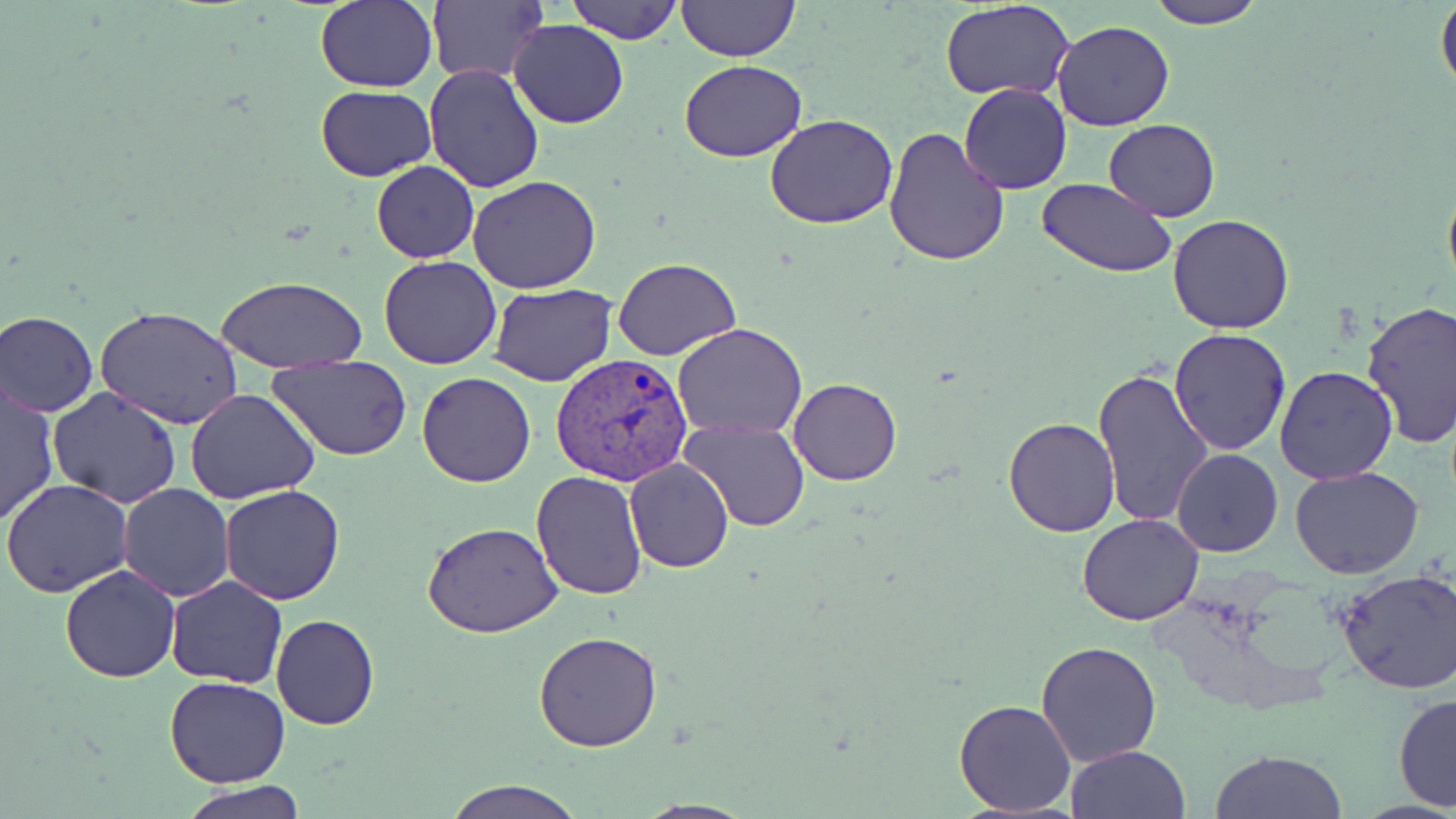
Summary:
  - Coordinate format: approximate bounding boxes as (x1,y1)-(x2,y2) corner pairs in pixels
  - Uninfected red blood cell locations: (315,0)-(436,92), (567,0)-(683,44), (1146,0)-(1266,29), (676,1)-(799,64), (941,1)-(1075,101), (1436,1)-(1456,96), (426,3)-(546,83), (508,20)-(630,129), (1052,20)-(1175,131), (680,60)-(805,163), (425,64)-(544,193), (959,84)-(1071,193), (316,85)-(437,181), (765,113)-(898,229), (1104,120)-(1222,219), (882,125)-(1012,268), (370,160)-(478,263), (1441,172)-(1456,302), (468,175)-(603,293), (1037,178)-(1176,276), (1167,214)-(1296,333), (378,256)-(503,369), (614,258)-(741,361), (218,277)-(369,375), (491,283)-(616,384), (1359,300)-(1456,448), (96,307)-(243,429), (1,309)-(98,417), (672,323)-(806,439), (1168,328)-(1293,457), (268,354)-(413,459), (1274,364)-(1399,484), (1093,365)-(1214,529), (417,372)-(535,487), (789,378)-(901,485), (1,383)-(60,528), (47,387)-(183,511), (185,388)-(319,505), (1003,416)-(1122,537), (679,418)-(810,532), (1172,449)-(1284,558), (624,457)-(733,573), (1290,467)-(1424,581), (532,469)-(649,599), (2,480)-(133,598), (118,484)-(235,602), (220,484)-(346,604), (1076,513)-(1204,625), (421,522)-(564,638), (59,564)-(181,682), (1336,569)-(1456,696), (166,577)-(289,689), (270,614)-(379,729), (533,632)-(661,753), (1037,642)-(1162,767), (164,676)-(292,787), (1392,692)-(1456,812), (952,699)-(1078,817), (1065,745)-(1190,819), (1208,748)-(1350,818), (442,778)-(585,818), (182,784)-(308,819)
  - Plasmodium vivax-infected red blood cell locations: (552,352)-(690,488)
  - Slide-level diagnosis: Plasmodium vivax
  - Field of view: one of a larger specimen
  - Modality: light microscopy
  - Magnification: 1000x
  - Image size: 1456×819 pixels
  - Stain: May-Grünwald-Giemsa
  - Preparation: thin blood smear